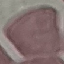
Summary:
  - Result: no malaria parasites detected
  - Capture: smartphone through the microscope eyepiece
  - Preparation: thin blood smear
  - Image type: cell patch, automatically extracted from a larger field of view and resized to 64 × 64 pixels
  - Stain: Giemsa